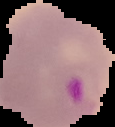
Summary:
  - Image type: cell region segmented out of the field of view; surrounding area masked to black
  - Image size: 115×127 pixels
  - Preparation: thin blood smear
  - Result: malaria parasites detected